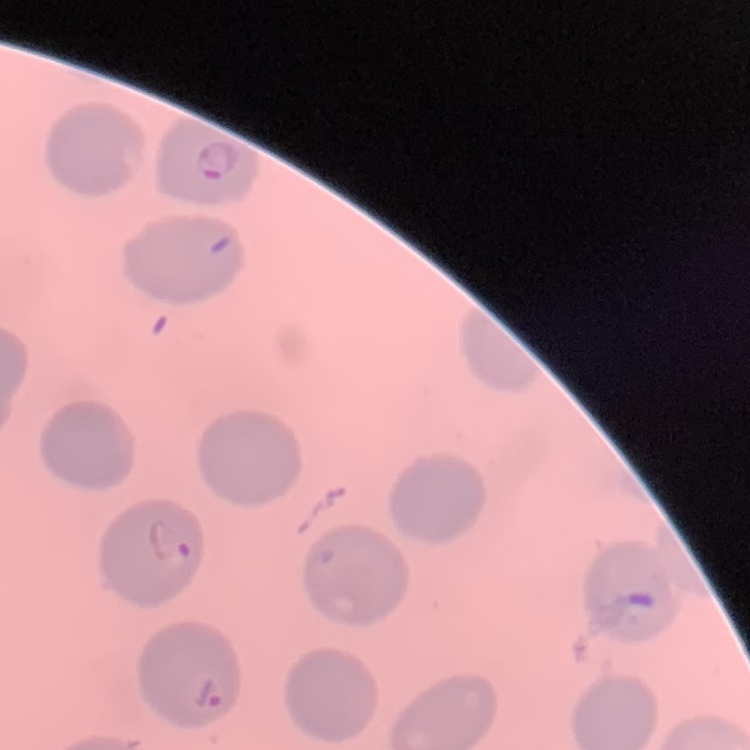
red blood cell morphology = no rouleaux formation
image type = square crop of a larger photomicrograph
preparation = thin peripheral smear
stain = Field's or Giemsa